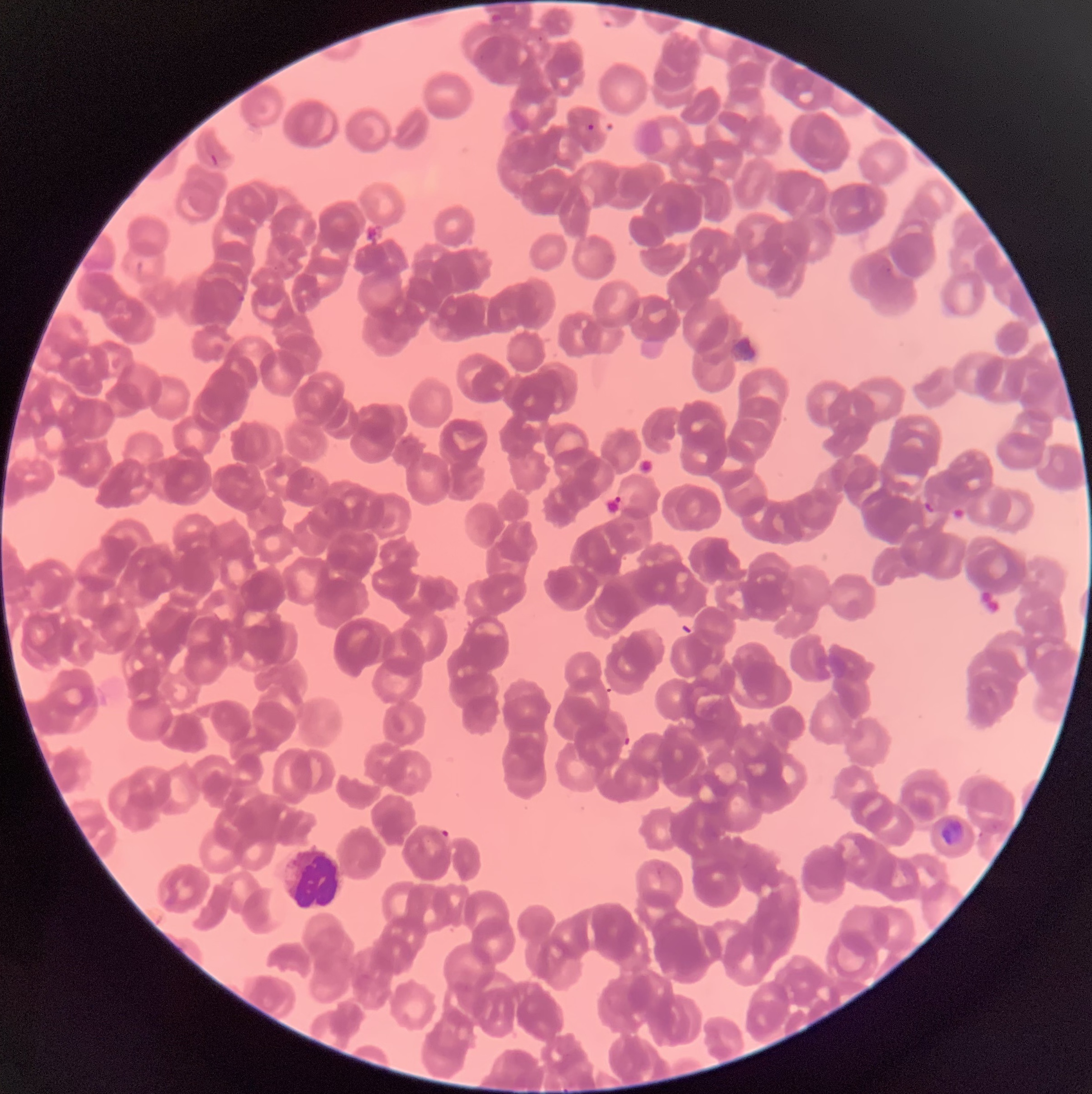

Approximate bounding boxes as [x1, y1, x2, y2] in pixels. Plasmodium parasite locations: [599, 9, 620, 31], [536, 35, 544, 47], [597, 110, 616, 136], [584, 121, 594, 132], [210, 152, 219, 167], [879, 263, 893, 280], [237, 292, 246, 305], [923, 499, 937, 514], [622, 735, 631, 747], [436, 827, 454, 847]. Optical microscopy. Thin blood smear. Image is 1092×1094 pixels. The red blood cells show rouleaux formation.